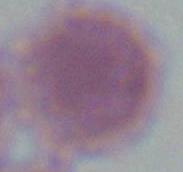

{
  "identification": "red blood cell",
  "modality": "micrograph",
  "magnification": "1000x"
}